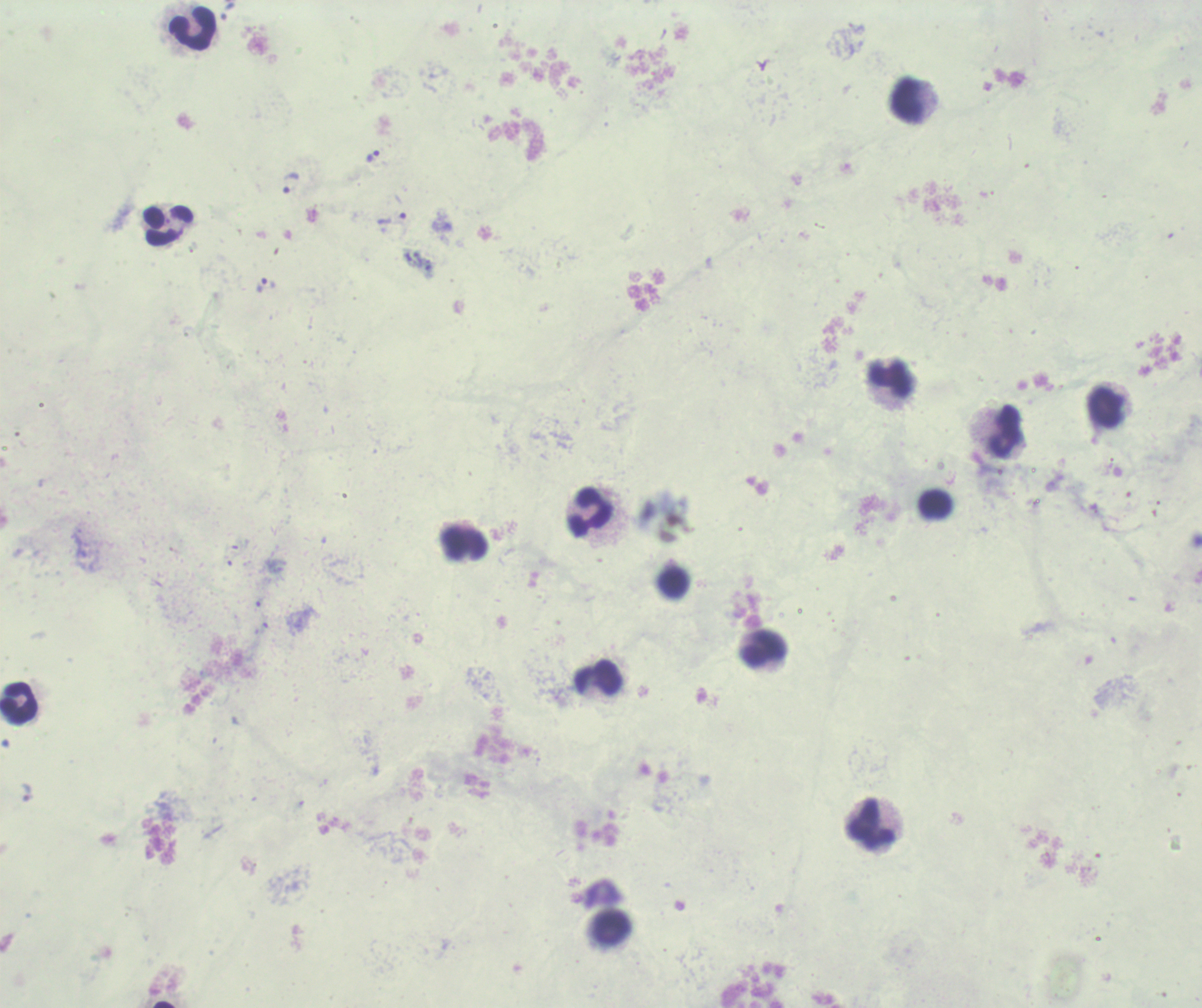

{
  "leukocyte_locations": "approximate centers as [x, y] in pixels: [192, 28], [907, 101], [169, 225], [889, 377], [1106, 408], [1006, 430], [935, 504], [591, 512], [465, 544], [673, 582], [765, 648], [599, 677], [19, 704], [871, 825], [611, 927]",
  "field_of_view": "single",
  "magnification": "100x",
  "background_quality": "poor",
  "stain": "Romanowsky",
  "image_size": "1202×1008 pixels",
  "result": "Plasmodium parasites detected",
  "trophozoite_locations": "approximate centers as [x, y] in pixels: [227, 12], [372, 156], [291, 182], [392, 219], [265, 286], [26, 792]",
  "preparation": "thick smear of blood",
  "context": "previously used in a real diagnosis"
}